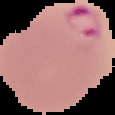
preparation: thin blood film
malaria_status: parasitized
image_type: segmented cell region with the area outside set to black
image_size: 115×115 pixels